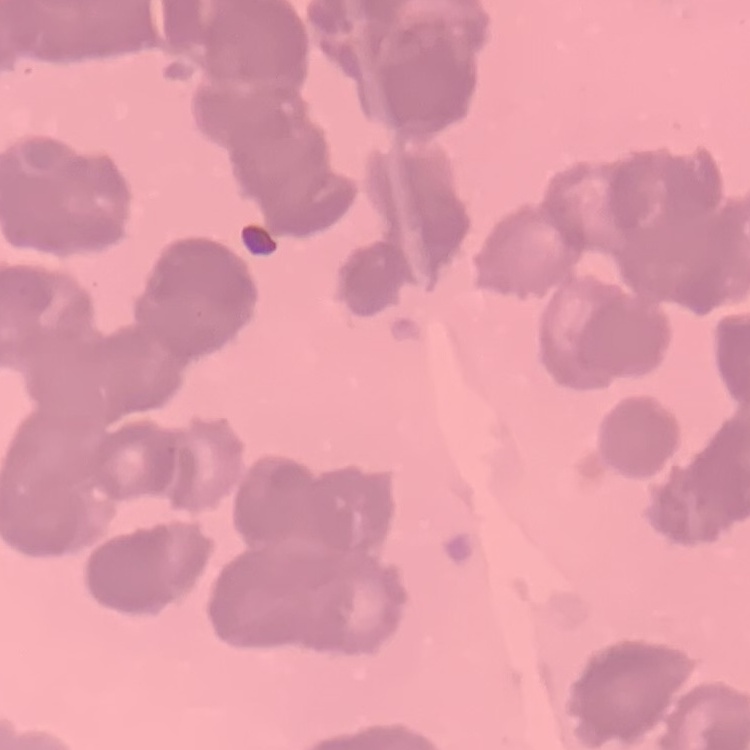

Summary:
  - Red blood cell morphology: rouleaux formation
  - Stain: Field's or Giemsa
  - Preparation: thin blood film
  - Image type: square crop of a larger photomicrograph